Report the malaria status of this cell.
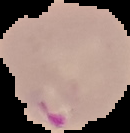
Parasitized.

preparation = thin blood smear
image size = 130×133 pixels
image type = segmented cell region with the area outside set to black